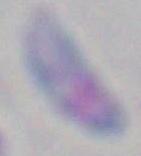

1000x magnification. Toxoplasma gondii is shown. Photomicrograph.